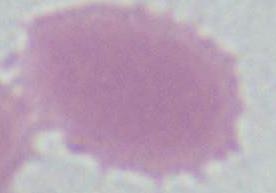

identification = erythrocyte
magnification = 1000x
modality = micrograph